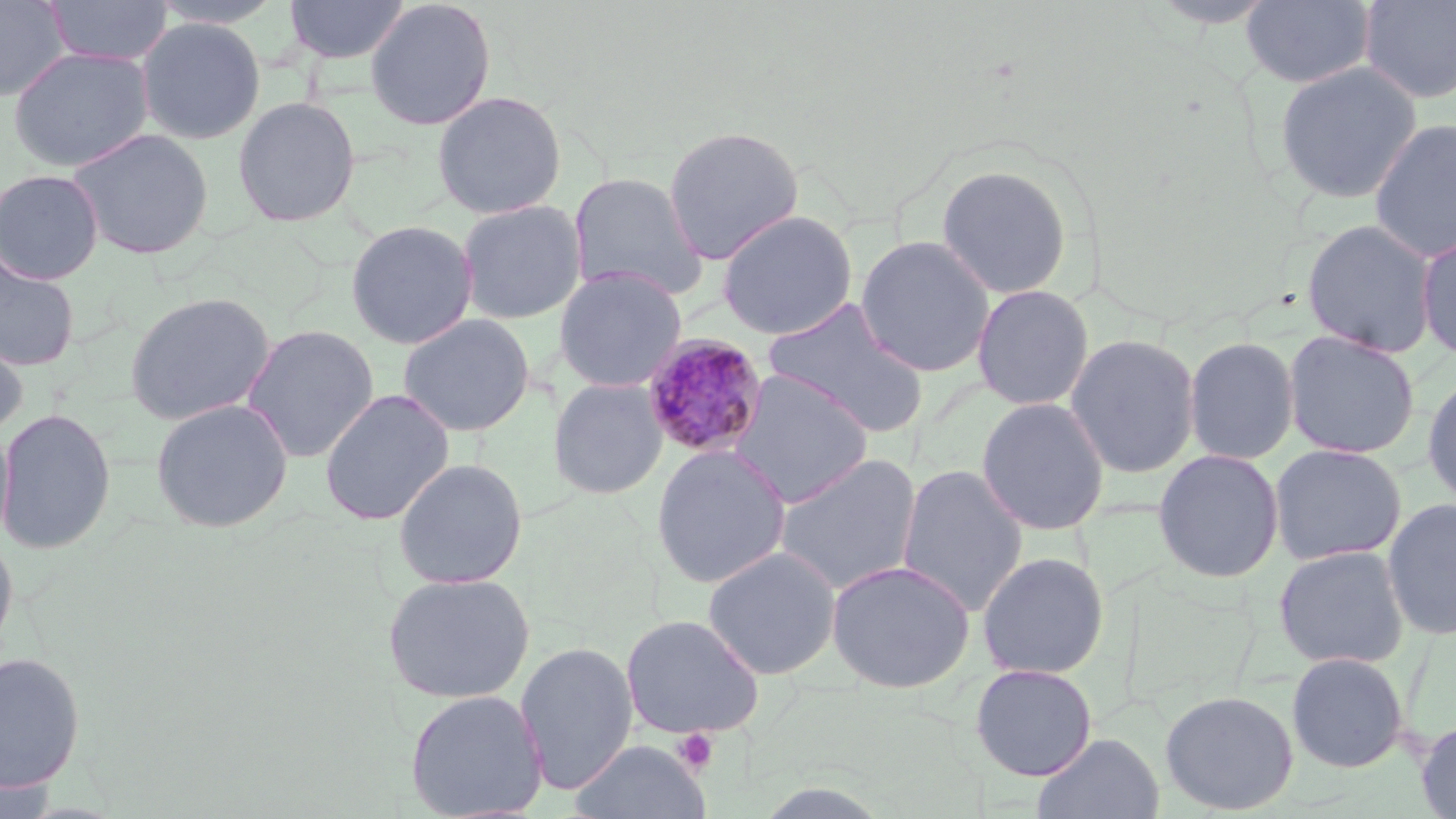
Approximate bounding boxes as (x1,y1)-(x2,y2) corner pairs in pixels. Platelet locations: (672,728)-(720,774). Uninfected red blood cell locations: (43,0)-(174,66), (284,0)-(409,64), (364,0)-(497,130), (1239,0)-(1377,89), (1358,0)-(1456,105), (0,1)-(72,101), (135,17)-(266,145), (7,45)-(154,172), (1274,60)-(1423,204), (432,90)-(567,219), (232,95)-(361,228), (1368,117)-(1456,262), (662,124)-(804,264), (66,127)-(215,260), (934,164)-(1073,299), (0,168)-(105,285), (567,171)-(709,302), (456,199)-(587,325), (716,209)-(859,340), (1300,218)-(1440,358), (344,219)-(479,350), (1416,233)-(1456,362), (855,234)-(996,378), (0,250)-(81,372), (553,267)-(688,393), (971,283)-(1095,411), (123,291)-(277,426), (762,298)-(930,438), (397,312)-(536,437), (240,324)-(380,463), (1282,329)-(1421,460), (0,330)-(29,441), (1064,333)-(1201,478), (1184,335)-(1300,466), (728,369)-(875,508), (1422,369)-(1456,510), (548,377)-(668,500), (318,388)-(455,526), (149,397)-(294,533), (975,397)-(1111,536), (0,406)-(117,555), (0,418)-(15,549), (1269,442)-(1407,566), (651,444)-(791,589), (1151,449)-(1285,583), (773,452)-(923,597), (392,457)-(529,589), (896,464)-(1029,616), (1382,497)-(1456,641), (0,526)-(19,667), (1272,544)-(1411,670), (702,545)-(841,680), (976,551)-(1110,679), (825,559)-(975,693), (382,571)-(535,704), (620,613)-(766,740), (515,641)-(638,794), (0,651)-(87,793), (1286,651)-(1410,773), (969,662)-(1098,781), (404,689)-(549,819), (1160,689)-(1299,815), (1416,718)-(1456,818), (1032,732)-(1165,819), (570,739)-(710,819). Plasmodium malariae-infected red blood cell locations: (640,333)-(770,460). Slide-level diagnosis: Plasmodium malariae. Image is 1456×819 pixels. Captured at 1000x magnification. One field of a larger specimen. May-Grünwald-Giemsa-stained preparation. Light microscopy. Thin blood film.